Evaluate for malaria.
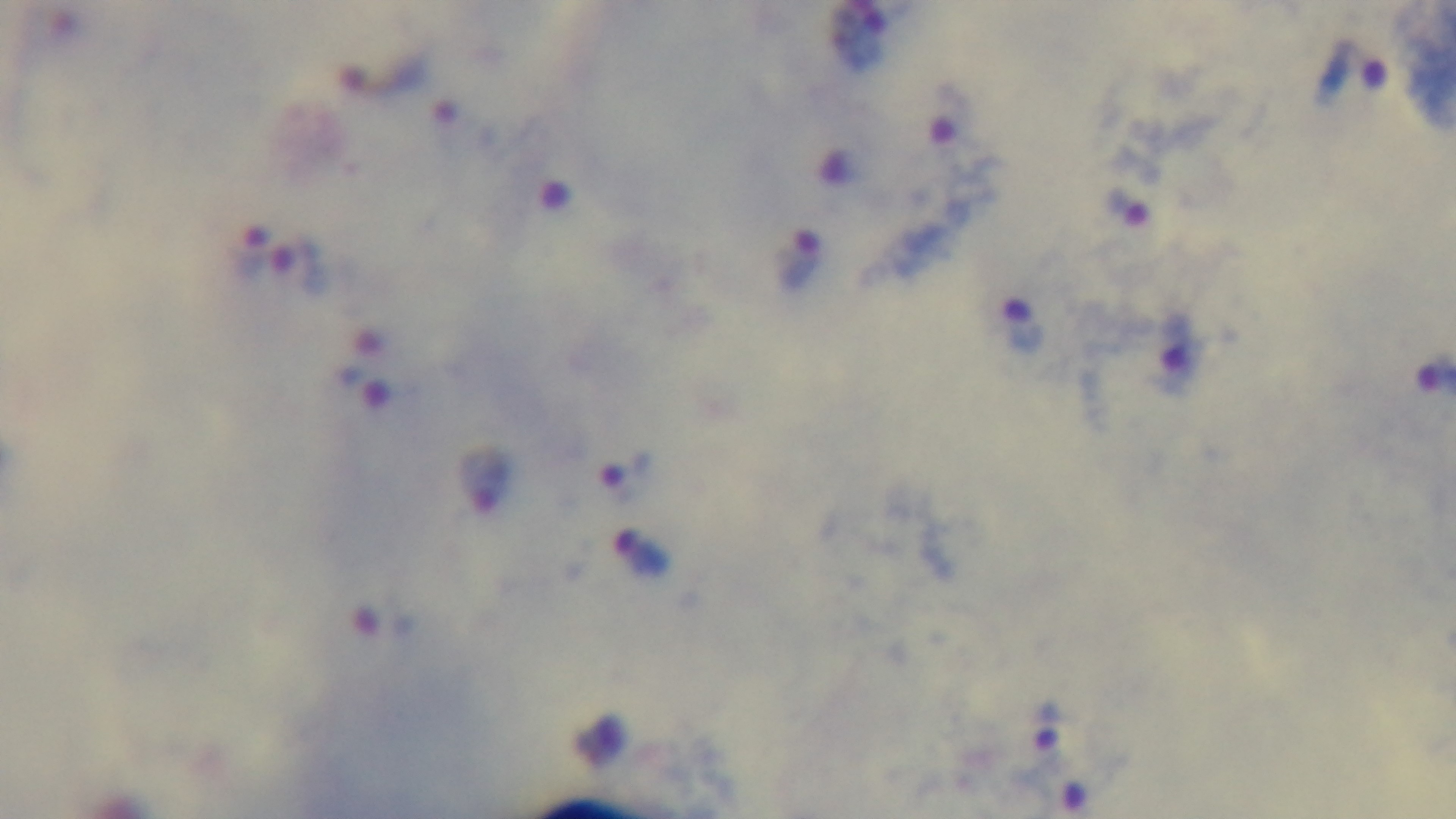

It is infected.

100x oil-immersion objective. Mounted 4K digital camera. Giemsa stain. Preparation: thick blood film. Single field of view. Photomicrograph.